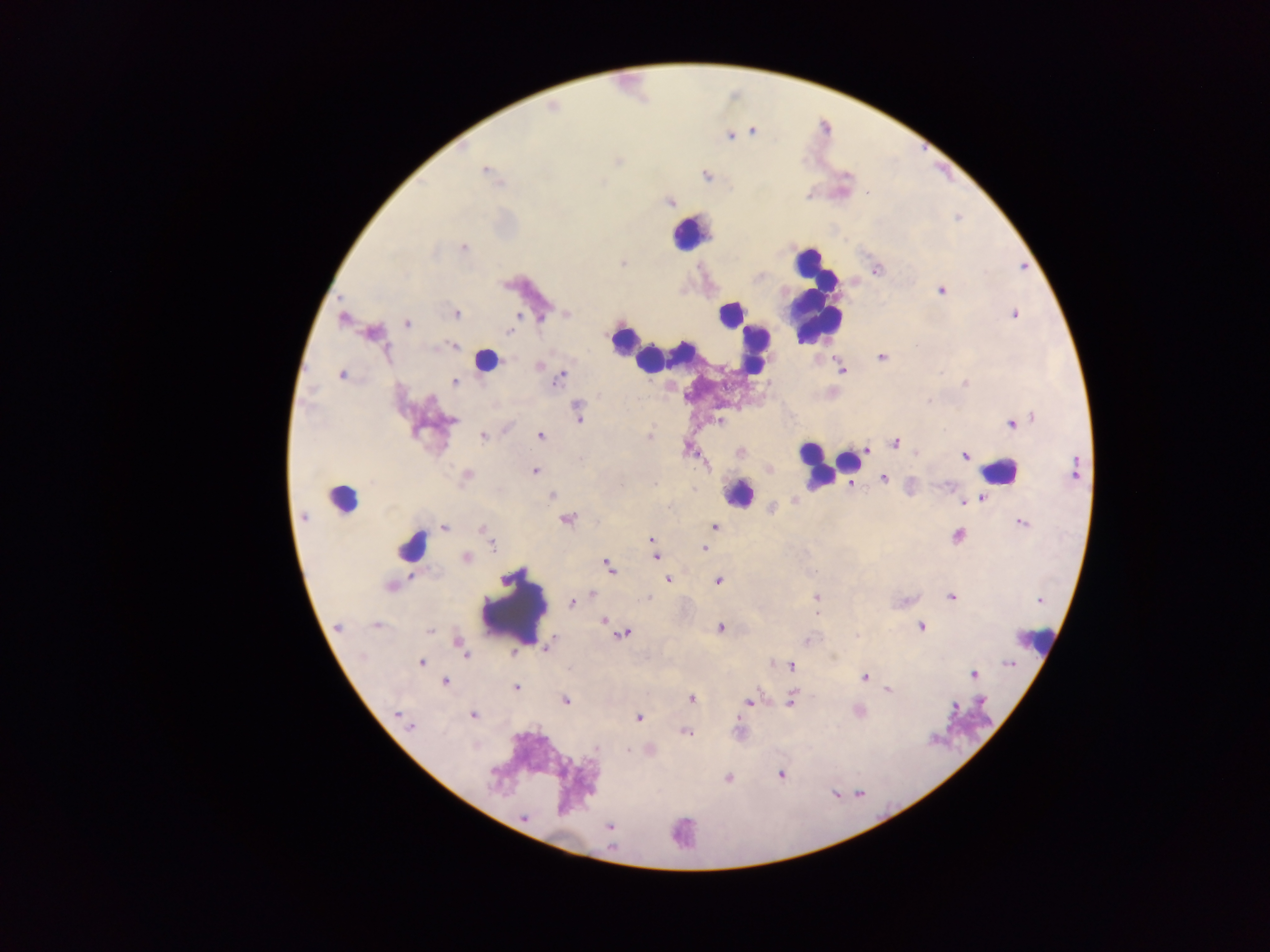
capture = mobile-phone photograph through a microscope
preparation = thick blood film
malaria parasite locations = approximate centers as (x, y) in pixels: (729, 136), (487, 173), (706, 176), (670, 202), (463, 247), (622, 263), (941, 290), (1013, 313), (456, 314), (567, 314), (541, 319), (342, 320), (407, 323), (510, 332), (450, 347), (882, 357), (539, 365), (841, 370), (342, 375), (560, 377), (454, 381), (578, 412), (451, 420), (720, 422), (1014, 423), (541, 436), (650, 436), (483, 437), (895, 443), (689, 450), (866, 450), (739, 452), (964, 455), (1074, 468), (535, 470), (466, 476), (884, 478), (621, 484), (553, 495), (981, 498), (772, 509), (303, 516), (567, 519), (1023, 524), (445, 527), (714, 527), (483, 529), (957, 535), (487, 536), (652, 541), (492, 544), (704, 548), (655, 555), (467, 558), (609, 566), (668, 579), (718, 581), (389, 586), (592, 594), (817, 597), (950, 597), (648, 599), (572, 603), (606, 621), (376, 625), (338, 627), (721, 627), (921, 627), (430, 631), (624, 633), (807, 639), (461, 646), (463, 652), (422, 662), (1009, 664), (791, 666), (973, 674), (864, 677), (445, 682), (516, 687), (889, 690), (692, 699), (791, 700), (566, 701), (750, 701), (982, 701), (955, 707), (474, 715), (399, 716), (638, 717), (410, 726), (686, 733), (781, 775), (728, 778), (524, 817), (609, 826)
image size = 1270×952 pixels
leukocyte locations = approximate centers as (x, y) in pixels: (688, 235), (814, 295), (729, 314), (622, 340), (754, 348), (485, 357), (649, 359), (849, 464), (815, 465), (1000, 472), (739, 493), (342, 497), (415, 545), (513, 607), (1042, 643)
field of view = single
country = Ghana